Locate every blood parasite and identify its species.
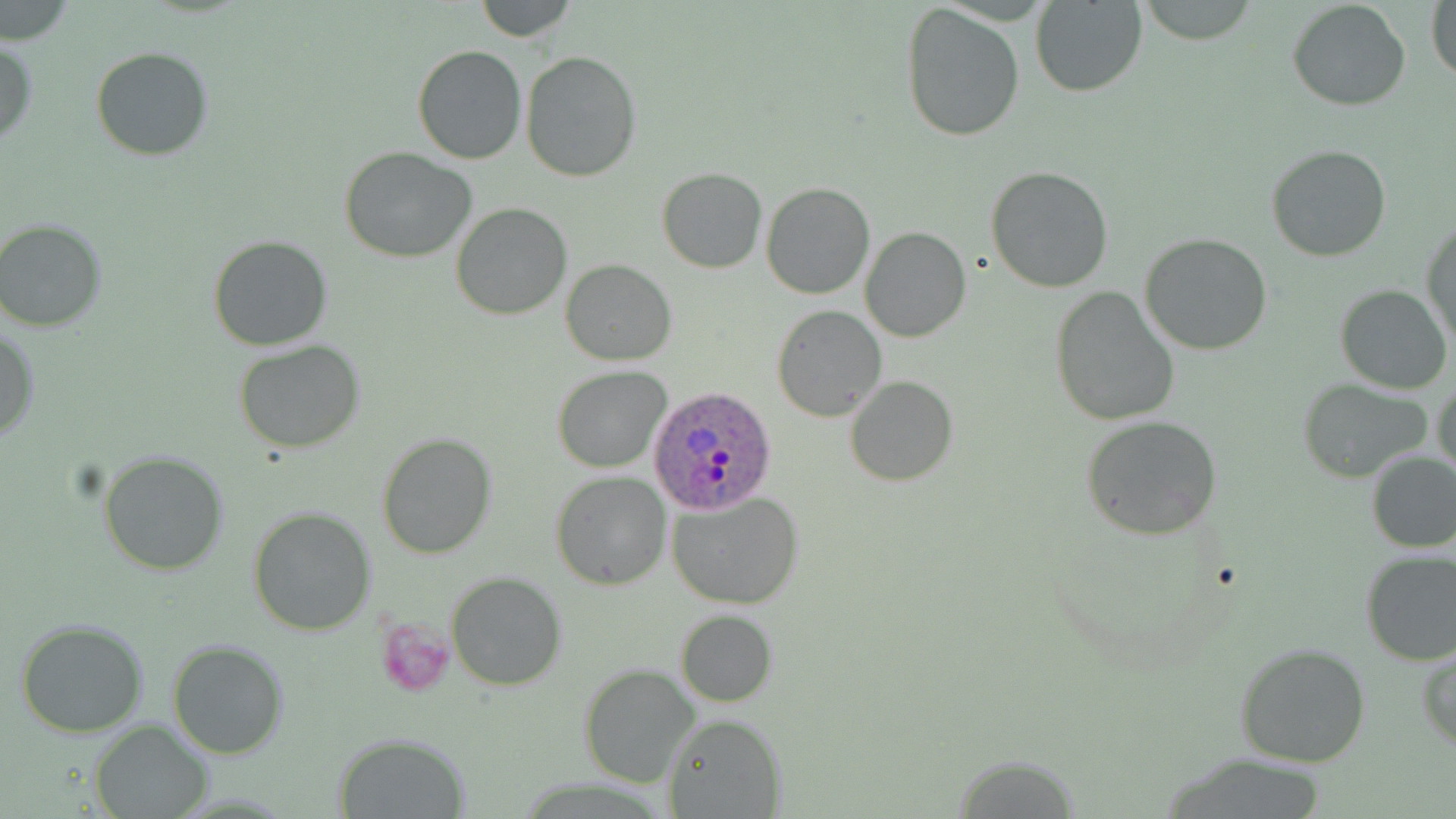
Approximate bounding boxes as (x1,y1)-(x2,y2) corner pairs in pixels.
Plasmodium ovale-infected red blood cells: (646,388)-(777,512).
No Plasmodium falciparum, Plasmodium malariae, Plasmodium vivax, Babesia divergens, or Trypanosoma brucei observed.

slide-level diagnosis = Plasmodium ovale
uninfected red blood cell locations = approximate bounding boxes as (x1,y1)-(x2,y2) corner pairs in pixels: (473,0)-(578,41), (1135,0)-(1257,43), (1427,0)-(1456,88), (1029,1)-(1146,97), (1287,1)-(1411,111), (900,3)-(1026,143), (0,38)-(37,146), (412,46)-(526,165), (91,47)-(215,162), (520,51)-(643,181), (1266,143)-(1394,262), (340,147)-(478,261), (985,166)-(1114,293), (657,168)-(768,274), (760,182)-(876,300), (450,202)-(572,320), (1,217)-(112,333), (1421,217)-(1455,351), (860,227)-(970,343), (1139,234)-(1273,356), (209,235)-(332,351), (561,259)-(675,366), (1335,284)-(1453,395), (1050,288)-(1179,426), (772,305)-(885,422), (1,325)-(38,444), (233,340)-(367,454), (552,364)-(671,474), (1432,374)-(1456,481), (846,376)-(958,487), (1299,378)-(1432,482), (1081,416)-(1222,540), (377,432)-(495,559), (99,449)-(231,576), (1364,451)-(1456,553), (551,471)-(671,589), (668,492)-(805,608), (247,507)-(376,636), (1359,549)-(1456,666), (446,571)-(566,691), (673,610)-(776,707), (14,618)-(150,736), (167,638)-(290,759), (1232,642)-(1372,769), (1418,646)-(1456,751), (580,663)-(702,789), (663,714)-(785,819), (89,719)-(213,818), (335,733)-(470,817), (947,752)-(1083,815)
image size = 1456×819 pixels
stain = May-Grünwald-Giemsa
magnification = 1000x
preparation = thin blood film
field of view = single
modality = light microscopy
platelet locations = approximate bounding boxes as (x1,y1)-(x2,y2) corner pairs in pixels: (377,619)-(454,696)